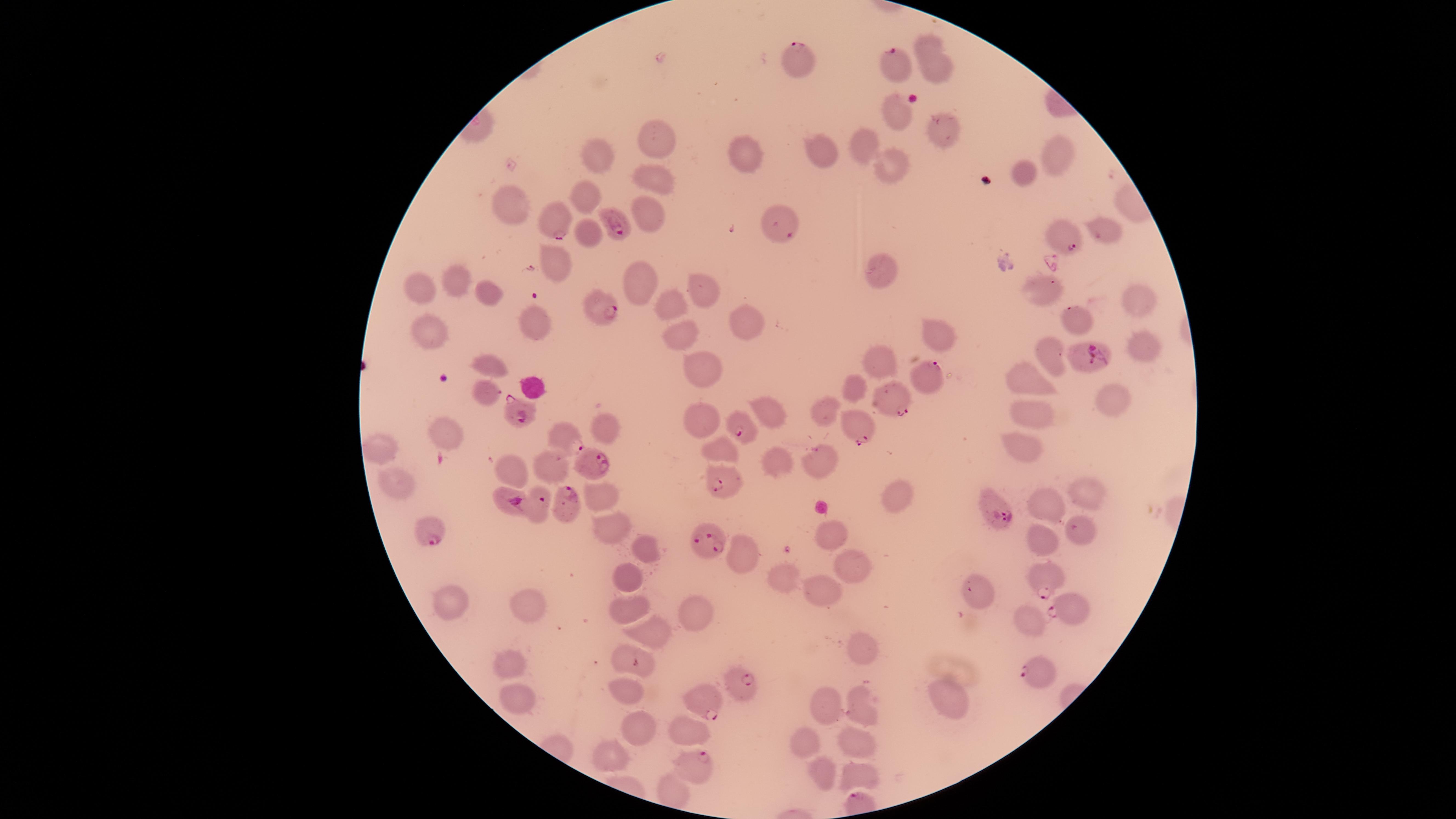
{
  "field_of_view": "single",
  "uninfected_red_blood_cells": "approximate marker points, in pixels from the top-left corner: (x=930, y=45), (x=933, y=67), (x=896, y=115), (x=942, y=128), (x=657, y=141), (x=862, y=144), (x=827, y=149), (x=744, y=150), (x=607, y=154), (x=1050, y=157), (x=891, y=166), (x=1024, y=171), (x=653, y=175), (x=587, y=192), (x=513, y=201), (x=651, y=219), (x=1099, y=233), (x=589, y=235), (x=555, y=259), (x=884, y=273), (x=642, y=278), (x=458, y=281), (x=1044, y=284), (x=425, y=286), (x=695, y=288), (x=491, y=293), (x=1135, y=302), (x=674, y=305), (x=1073, y=312), (x=531, y=316), (x=745, y=320), (x=433, y=326), (x=938, y=332), (x=682, y=334), (x=1145, y=343), (x=1056, y=351), (x=886, y=360), (x=490, y=365), (x=704, y=367), (x=1026, y=377), (x=861, y=383), (x=487, y=392), (x=1105, y=398), (x=832, y=405), (x=766, y=408), (x=1039, y=410), (x=700, y=413), (x=599, y=424), (x=443, y=434), (x=386, y=445), (x=1021, y=446), (x=718, y=450), (x=511, y=464), (x=553, y=464), (x=778, y=464), (x=829, y=466), (x=393, y=480), (x=1087, y=491), (x=605, y=494), (x=894, y=499), (x=1050, y=505), (x=609, y=527), (x=1077, y=530), (x=831, y=531), (x=1044, y=539), (x=639, y=546), (x=740, y=550), (x=855, y=563), (x=626, y=573), (x=784, y=580), (x=829, y=589), (x=980, y=594), (x=528, y=606), (x=631, y=606), (x=450, y=608), (x=693, y=609), (x=1030, y=616), (x=648, y=628), (x=863, y=651), (x=636, y=655), (x=508, y=663), (x=632, y=686), (x=515, y=694), (x=943, y=699), (x=861, y=704), (x=828, y=705), (x=638, y=721), (x=690, y=734), (x=804, y=738), (x=855, y=747), (x=614, y=754), (x=827, y=773), (x=856, y=776), (x=672, y=788)",
  "presence": "malaria parasites identified",
  "species": "Plasmodium falciparum",
  "parasitized_red_blood_cells": "approximate marker points, in pixels from the top-left corner: (x=799, y=61), (x=893, y=66), (x=618, y=221), (x=563, y=222), (x=781, y=224), (x=1063, y=237), (x=604, y=311), (x=1087, y=358), (x=932, y=374), (x=890, y=397), (x=518, y=409), (x=860, y=426), (x=744, y=430), (x=567, y=438), (x=596, y=458), (x=723, y=482), (x=565, y=500), (x=506, y=502), (x=541, y=505), (x=995, y=510), (x=429, y=529), (x=706, y=540), (x=1042, y=575), (x=1071, y=609), (x=1038, y=673), (x=743, y=686), (x=702, y=702), (x=697, y=763)",
  "visible_region": "circular",
  "preparation": "thin smear of blood",
  "capture": "smartphone photograph through the microscope eyepiece",
  "image_size": "1456×819 pixels",
  "stain": "Giemsa"
}